Describe the morphology of the erythrocytes.
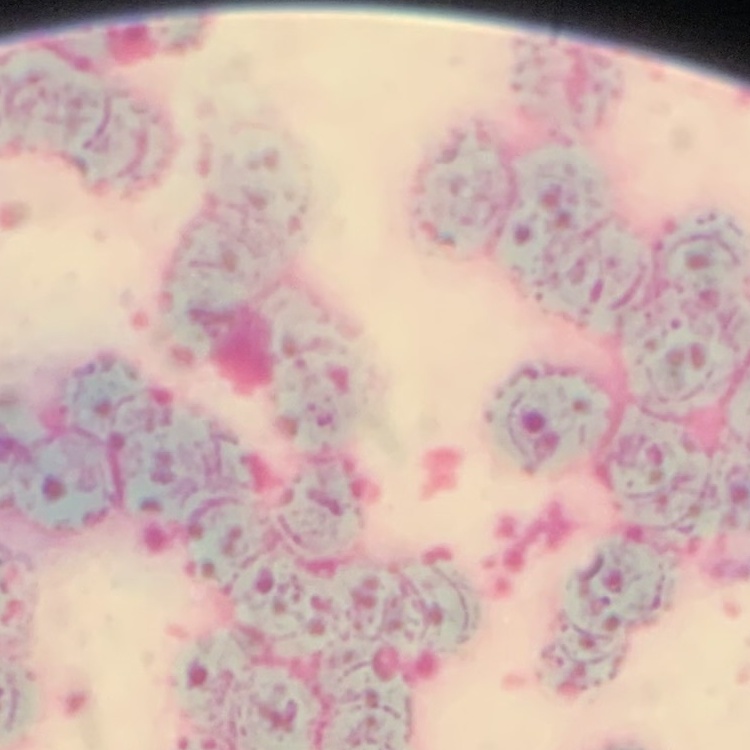
They show rouleaux formation.

image type = one tile cut from a larger photomicrograph
preparation = thin blood smear
stain = Field's or Giemsa